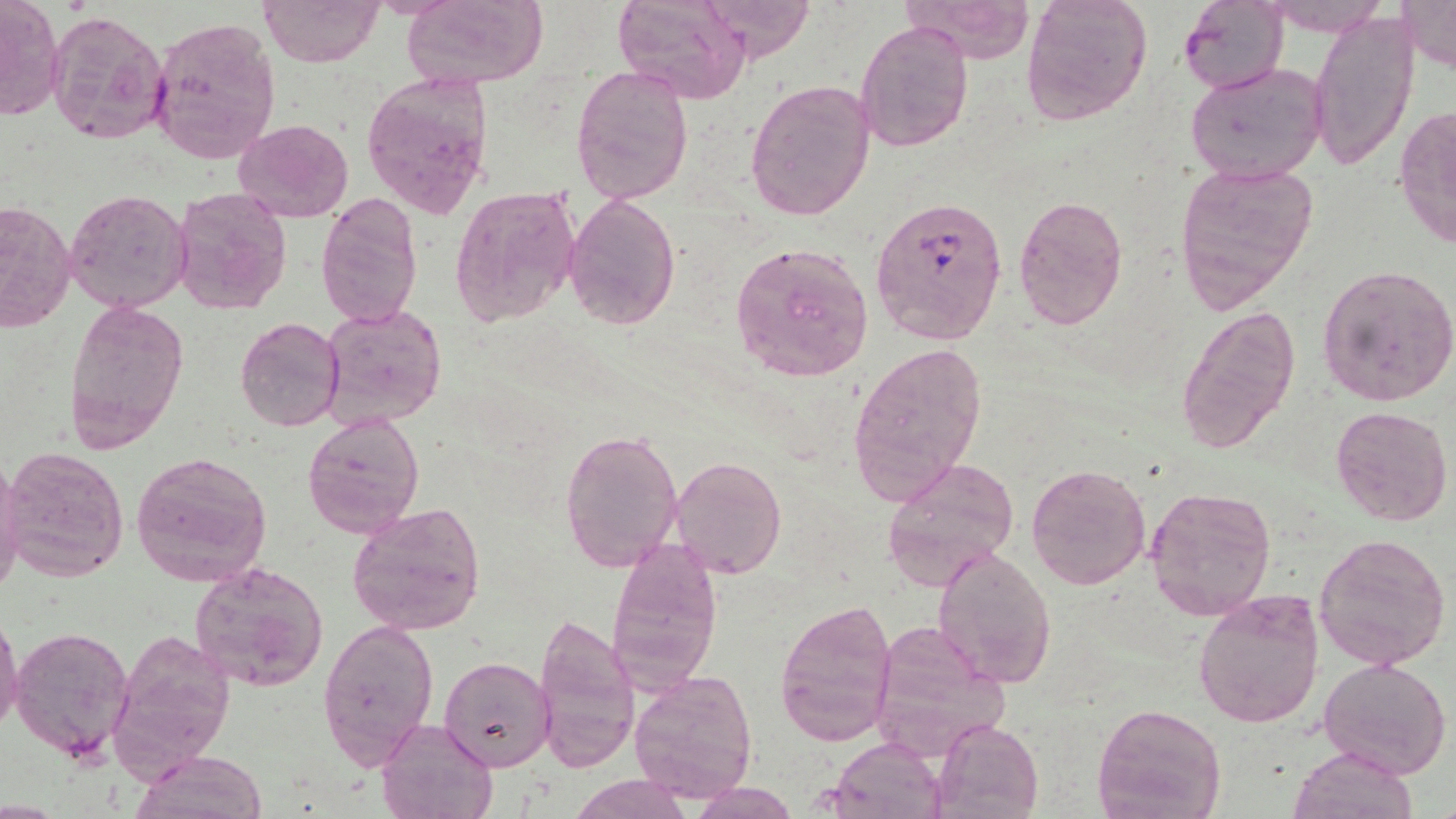
Summary:
  - Coordinate format: approximate bounding boxes as (x1,y1)-(x2,y2) corner pairs in pixels
  - Uninfected red blood cell locations: (1,0)-(64,122), (401,0)-(549,90), (612,0)-(751,103), (698,0)-(817,64), (1019,0)-(1152,124), (1178,0)-(1288,95), (1398,0)-(1456,73), (258,1)-(382,67), (905,1)-(1034,62), (46,7)-(170,149), (1308,9)-(1418,173), (147,17)-(281,163), (857,20)-(973,153), (1186,61)-(1330,186), (571,65)-(694,205), (359,69)-(493,221), (745,77)-(876,222), (1394,104)-(1456,249), (233,118)-(355,223), (1173,160)-(1320,311), (449,183)-(582,326), (171,187)-(293,315), (65,188)-(193,314), (565,191)-(680,330), (317,195)-(422,328), (1014,196)-(1128,329), (0,202)-(74,333), (729,240)-(873,381), (1317,265)-(1456,407), (64,296)-(189,453), (320,302)-(448,432), (1175,304)-(1299,457), (235,317)-(345,432), (848,341)-(989,503), (1331,405)-(1454,528), (301,408)-(424,538), (560,426)-(685,572), (3,447)-(130,582), (131,451)-(272,587), (670,454)-(789,580), (882,457)-(1018,590), (0,462)-(26,601), (1024,462)-(1150,592), (1143,484)-(1277,620), (347,502)-(486,635), (1314,531)-(1452,671), (605,538)-(724,694), (931,546)-(1056,689), (190,561)-(329,692), (1192,588)-(1325,728), (774,598)-(898,746), (533,611)-(643,775), (0,613)-(25,736), (317,618)-(438,769), (866,622)-(1007,758), (10,625)-(134,763), (109,627)-(237,781), (441,655)-(554,771), (1319,659)-(1451,778), (629,670)-(758,803), (1093,702)-(1226,818), (377,716)-(497,819), (932,719)-(1043,817), (827,736)-(948,819), (1289,746)-(1418,819), (134,751)-(270,819), (571,774)-(692,818), (690,779)-(799,818)
  - Plasmodium falciparum-infected red blood cell locations: (869,195)-(1007,345)
  - Slide-level diagnosis: Plasmodium falciparum
  - Stain: May-Grünwald-Giemsa
  - Field of view: one of a larger specimen
  - Preparation: thin blood film
  - Magnification: 1000x
  - Modality: light microscopy
  - Image size: 1456×819 pixels